State the blood parasite species.
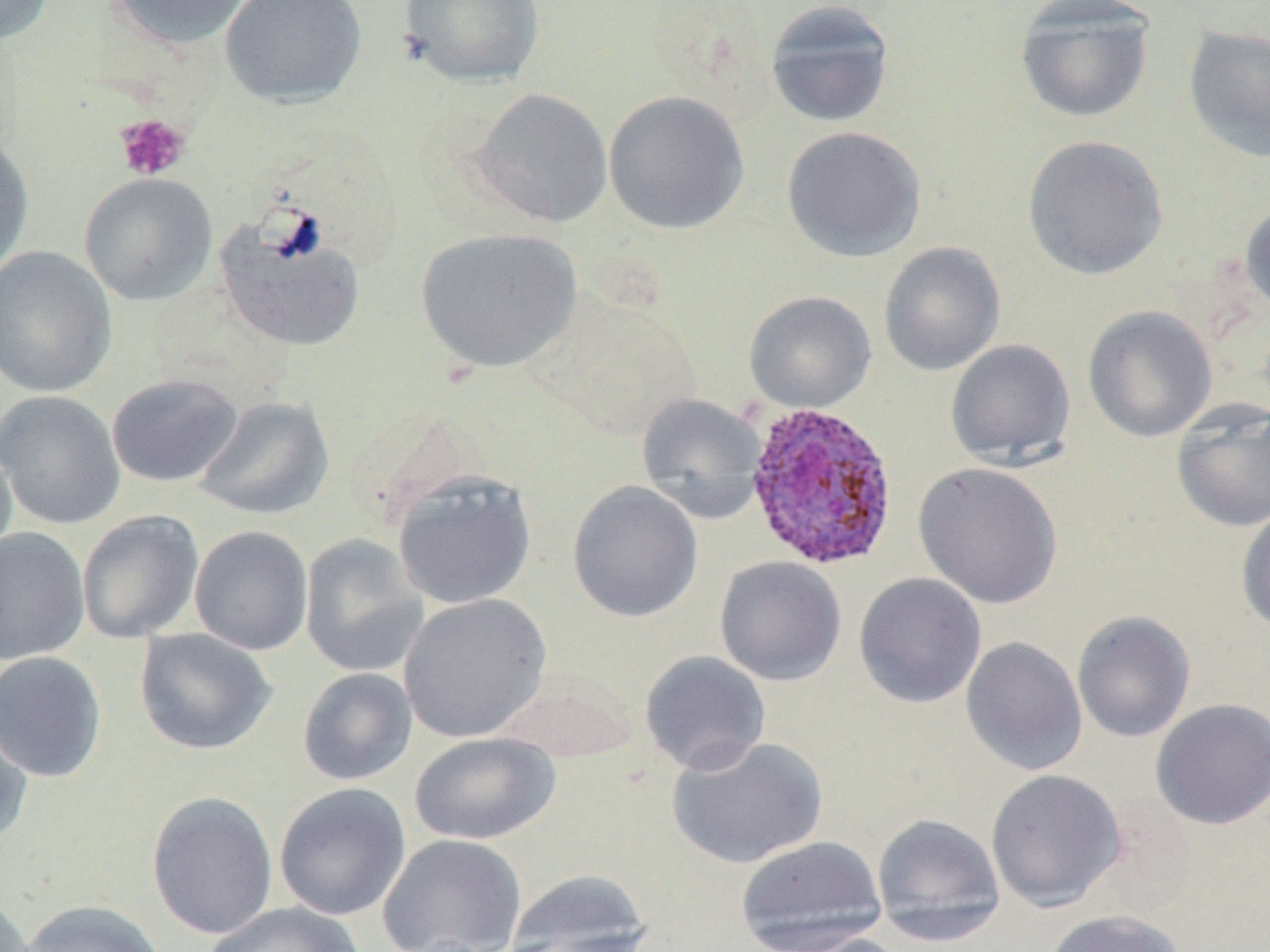
Plasmodium ovale.

preparation = thin blood smear
modality = optical microscopy
platelet locations = approximate bounding boxes as (x1, y1, x2, y2) in pixels: (114, 113, 191, 182)
uninfected red blood cell locations = approximate bounding boxes as (x1, y1, x2, y2) in pixels: (1, 0, 56, 45), (105, 0, 258, 51), (219, 0, 366, 108), (398, 0, 545, 88), (764, 1, 896, 128), (1015, 2, 1154, 124), (1182, 26, 1270, 163), (470, 87, 614, 229), (603, 90, 750, 235), (781, 125, 927, 263), (0, 132, 34, 279), (1022, 134, 1168, 281), (78, 172, 218, 306), (1239, 199, 1270, 317), (216, 217, 366, 352), (414, 227, 582, 374), (879, 241, 1006, 376), (0, 246, 118, 398), (743, 291, 877, 413), (531, 292, 698, 442), (1082, 305, 1217, 443), (945, 339, 1076, 469), (105, 373, 244, 488), (0, 390, 126, 531), (636, 393, 767, 523), (194, 395, 335, 520), (1170, 399, 1270, 533), (0, 433, 17, 567), (913, 461, 1063, 609), (392, 470, 537, 610), (567, 480, 703, 623), (1235, 503, 1270, 635), (76, 509, 205, 644), (189, 525, 314, 655), (0, 527, 90, 664), (299, 534, 428, 678), (714, 555, 847, 686), (854, 572, 987, 709), (398, 592, 552, 742), (1071, 610, 1196, 743), (134, 628, 278, 755), (961, 636, 1088, 776), (0, 650, 107, 783), (638, 650, 772, 776), (297, 667, 417, 786), (497, 671, 639, 763), (1151, 697, 1270, 830), (0, 711, 33, 849), (409, 732, 560, 844), (666, 735, 828, 869), (985, 769, 1127, 911), (273, 782, 411, 921), (145, 790, 279, 941), (871, 812, 1006, 945), (377, 833, 527, 952), (735, 835, 888, 952), (502, 868, 654, 951), (0, 891, 35, 952), (20, 899, 167, 952), (203, 901, 367, 952), (1041, 909, 1186, 952), (767, 930, 910, 952)
field of view = single
Plasmodium ovale-infected red blood cell locations = approximate bounding boxes as (x1, y1, x2, y2) in pixels: (744, 401, 900, 570)
stain = May-Grünwald-Giemsa
magnification = 1000x
image size = 1270×952 pixels